Assess the morphology of the red blood cells.
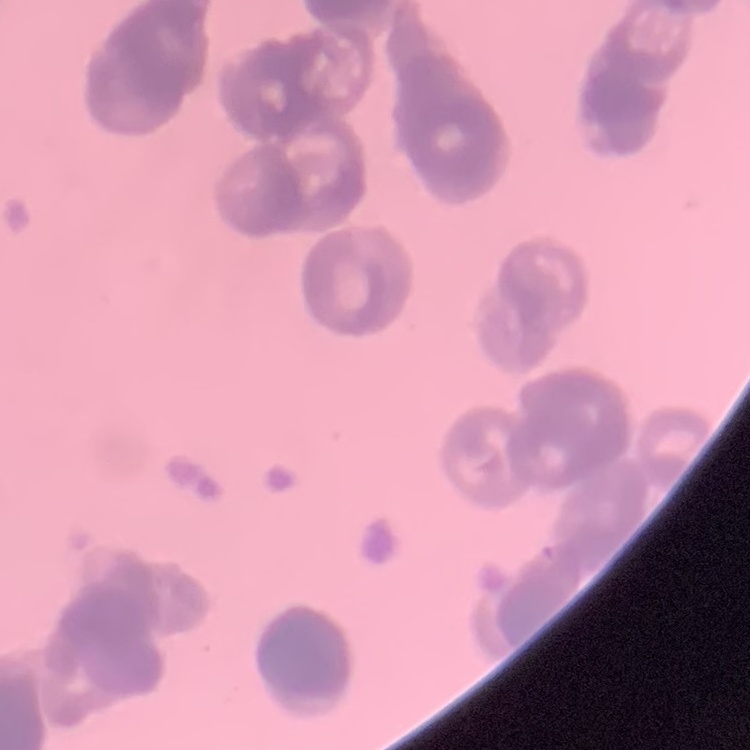

They show rouleaux formation.

Summary:
  - Stain: Field's or Giemsa
  - Image type: square crop of a larger photomicrograph
  - Preparation: thin blood film